Classify this cell by malaria status.
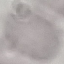
Uninfected.

Cell patch, automatically extracted from a larger field of view and resized to 64 × 64 pixels. Acquired by smartphone through the microscope eyepiece. Thin blood film. Giemsa-stained preparation.